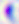

{
  "modality": "micrograph",
  "identification": "Toxoplasma gondii",
  "magnification": "400x"
}